Report the malaria status of this cell.
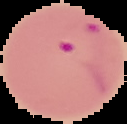

Parasitized.

image type = cell region segmented out of the field of view; surrounding area masked to black
preparation = thin blood smear
image size = 127×124 pixels